Give the position of every malaria parasite.
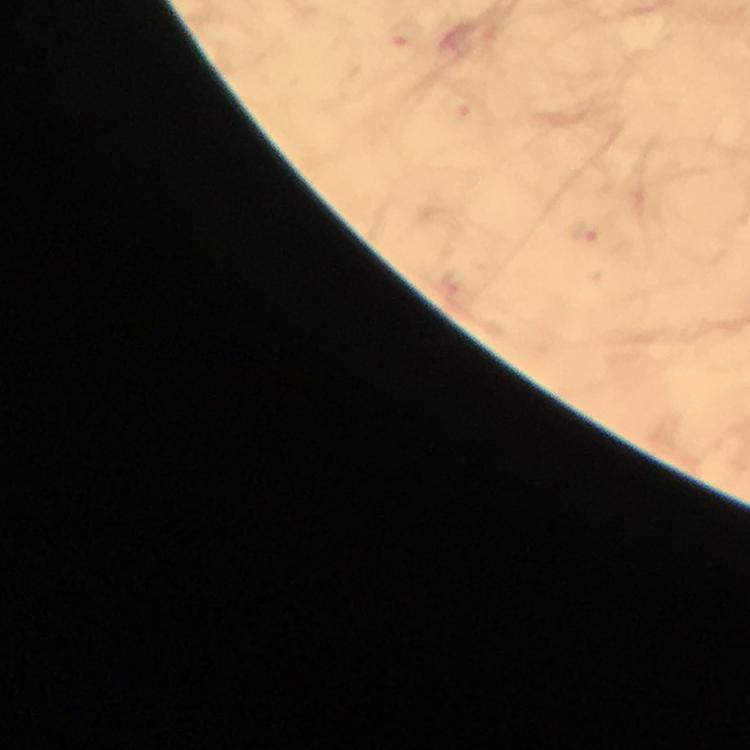
Approximate object centers, in pixels from the top-left corner.
Malaria parasites: (x=409, y=34).

Image is 750×750 pixels. Photographed through the microscope with a smartphone camera. Cropped region of a single field of view. From a diagnostic examination for malaria. Immersion oil applied. Thick smear. At 100x magnification. Giemsa-stained preparation.